Classify this cell by malaria status.
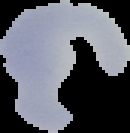
Uninfected.

The area outside the segmented cell region is set to black. From a thin blood film. Image is 130×133 pixels.